Assess this cell for malaria.
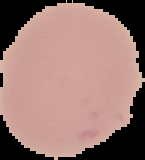
Uninfected.

Summary:
  - Image type: segmented cell region with the area outside set to black
  - Image size: 145×160 pixels
  - Preparation: thin blood smear